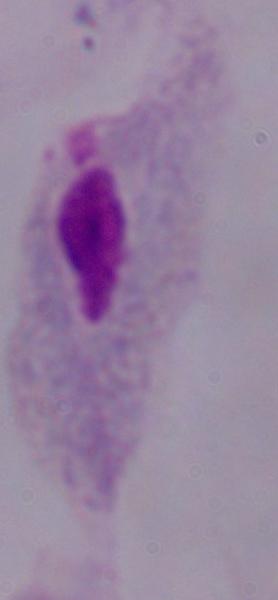 A trichomonad is seen. Captured at 1000x magnification. Micrograph.